State which parasite is depicted.
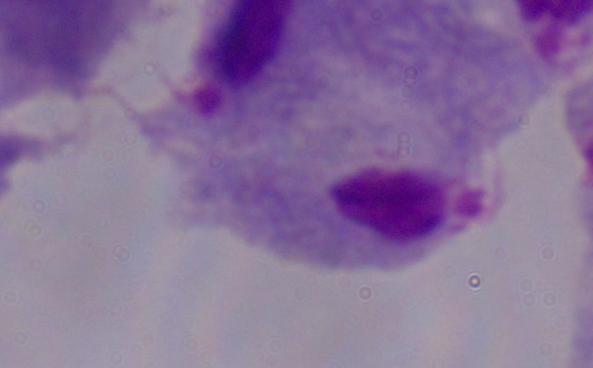
A trichomonad.

Summary:
  - Magnification: 1000x
  - Modality: photomicrograph